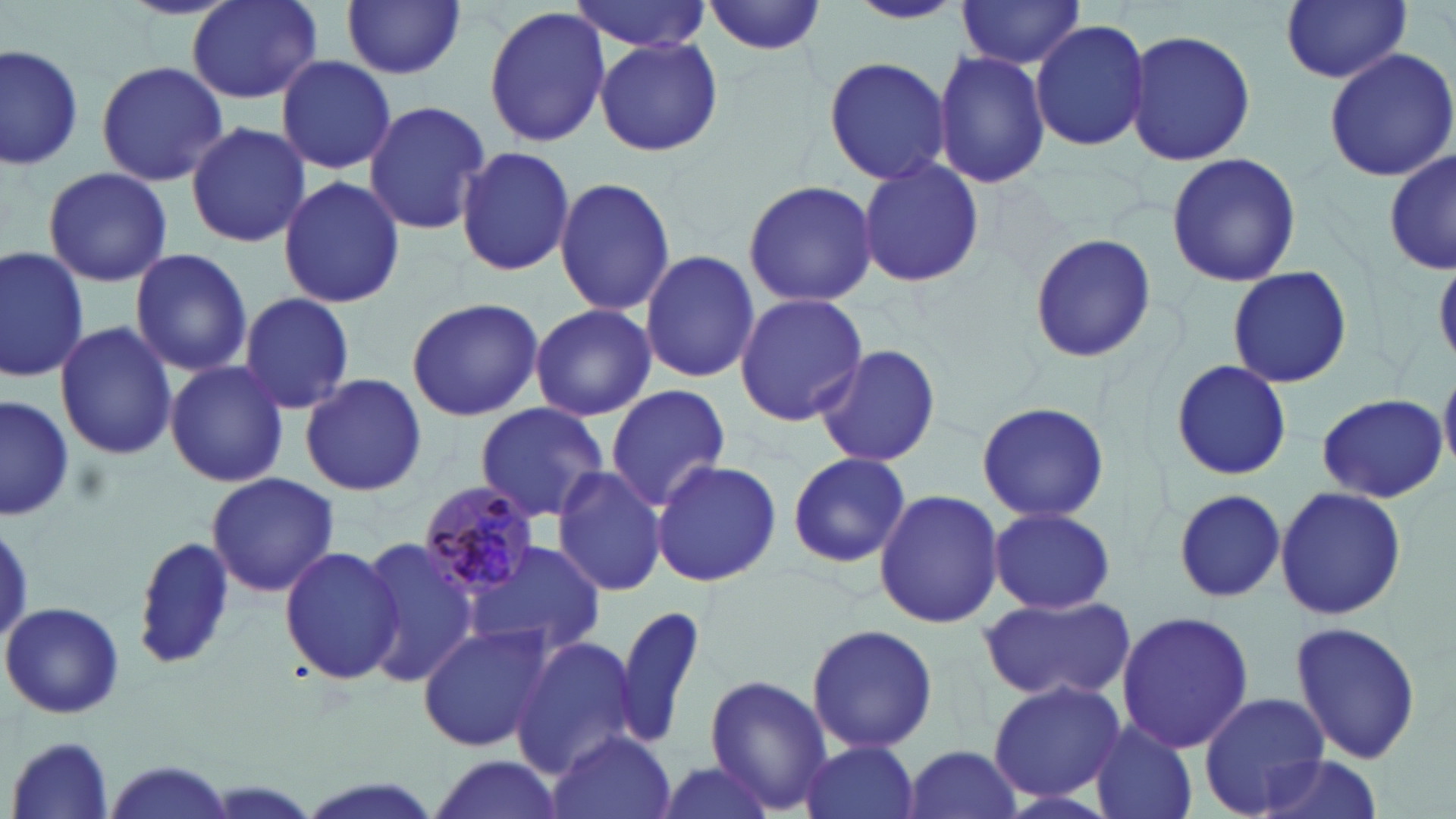

Summary:
  - Coordinate format: approximate bounding boxes as (x1,y1)-(x2,y2) corner pairs in pixels
  - Plasmodium malariae-infected red blood cell locations: (416,480)-(543,600)
  - Uninfected red blood cell locations: (185,0)-(324,102), (341,0)-(465,80), (569,0)-(711,54), (705,0)-(829,56), (844,0)-(966,25), (1278,0)-(1412,88), (954,1)-(1088,71), (482,6)-(612,148), (1030,19)-(1151,152), (1125,26)-(1256,169), (594,37)-(723,157), (1,41)-(85,174), (1323,48)-(1456,180), (933,49)-(1050,188), (275,55)-(397,174), (822,55)-(954,185), (94,59)-(227,185), (364,100)-(490,236), (184,119)-(309,249), (456,144)-(576,278), (1385,148)-(1456,278), (1164,151)-(1303,288), (855,159)-(985,288), (40,167)-(173,286), (277,174)-(405,309), (554,175)-(675,317), (741,178)-(878,308), (1027,233)-(1157,363), (0,243)-(91,382), (129,247)-(252,376), (640,248)-(760,384), (1226,265)-(1353,390), (239,292)-(357,414), (733,292)-(869,428), (406,297)-(545,422), (529,303)-(657,422), (54,319)-(179,462), (814,344)-(942,468), (1170,358)-(1292,482), (165,360)-(290,487), (1440,366)-(1456,473), (299,372)-(428,497), (604,384)-(733,509), (0,392)-(73,524), (1315,393)-(1450,502), (474,401)-(611,522), (976,401)-(1110,526), (786,453)-(912,570), (650,457)-(781,589), (550,465)-(666,598), (206,472)-(338,598), (1274,487)-(1406,619), (873,489)-(1003,629), (1172,489)-(1285,605), (987,507)-(1116,614), (133,537)-(237,671), (357,537)-(483,688), (463,540)-(608,661), (280,545)-(407,686), (979,592)-(1135,704), (0,601)-(125,720), (614,601)-(705,752), (1116,609)-(1253,756), (1288,621)-(1424,765), (806,623)-(939,754), (418,624)-(554,753), (511,635)-(642,776), (703,674)-(832,813), (987,679)-(1127,803), (1198,692)-(1328,815), (1088,721)-(1199,819), (548,729)-(677,819), (7,734)-(116,818), (798,738)-(922,819), (903,744)-(1025,819), (424,754)-(563,819), (1249,754)-(1386,819), (648,756)-(780,819), (96,760)-(236,819), (290,775)-(451,819)
  - Slide-level diagnosis: Plasmodium malariae
  - Magnification: 1000x
  - Image size: 1456×819 pixels
  - Preparation: thin blood smear
  - Field of view: single
  - Modality: light microscopy
  - Stain: May-Grünwald-Giemsa